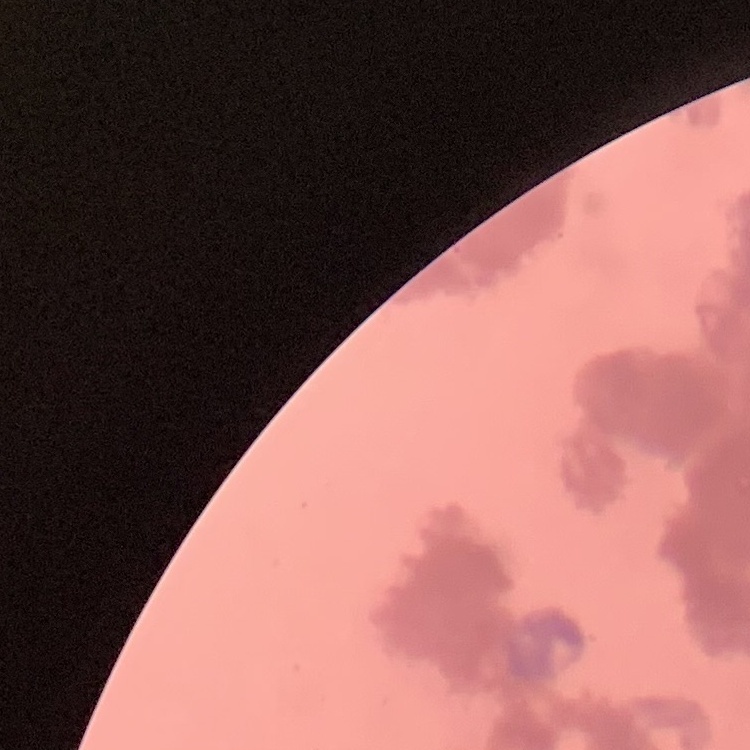

red blood cell morphology = rouleaux formation
stain = Field's or Giemsa
image type = square crop of a larger photomicrograph
preparation = thin blood film